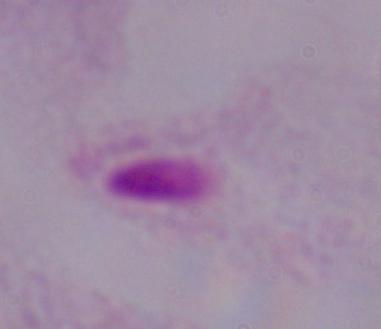
{
  "identification": "trichomonad",
  "magnification": "1000x",
  "modality": "photomicrograph"
}